Assess this cell for malaria.
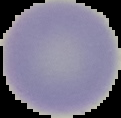

Uninfected.

From a thin blood film. The area outside the segmented cell region is set to black. Image is 121×118 pixels.